Outline each Plasmodium vivax-infected red blood cell.
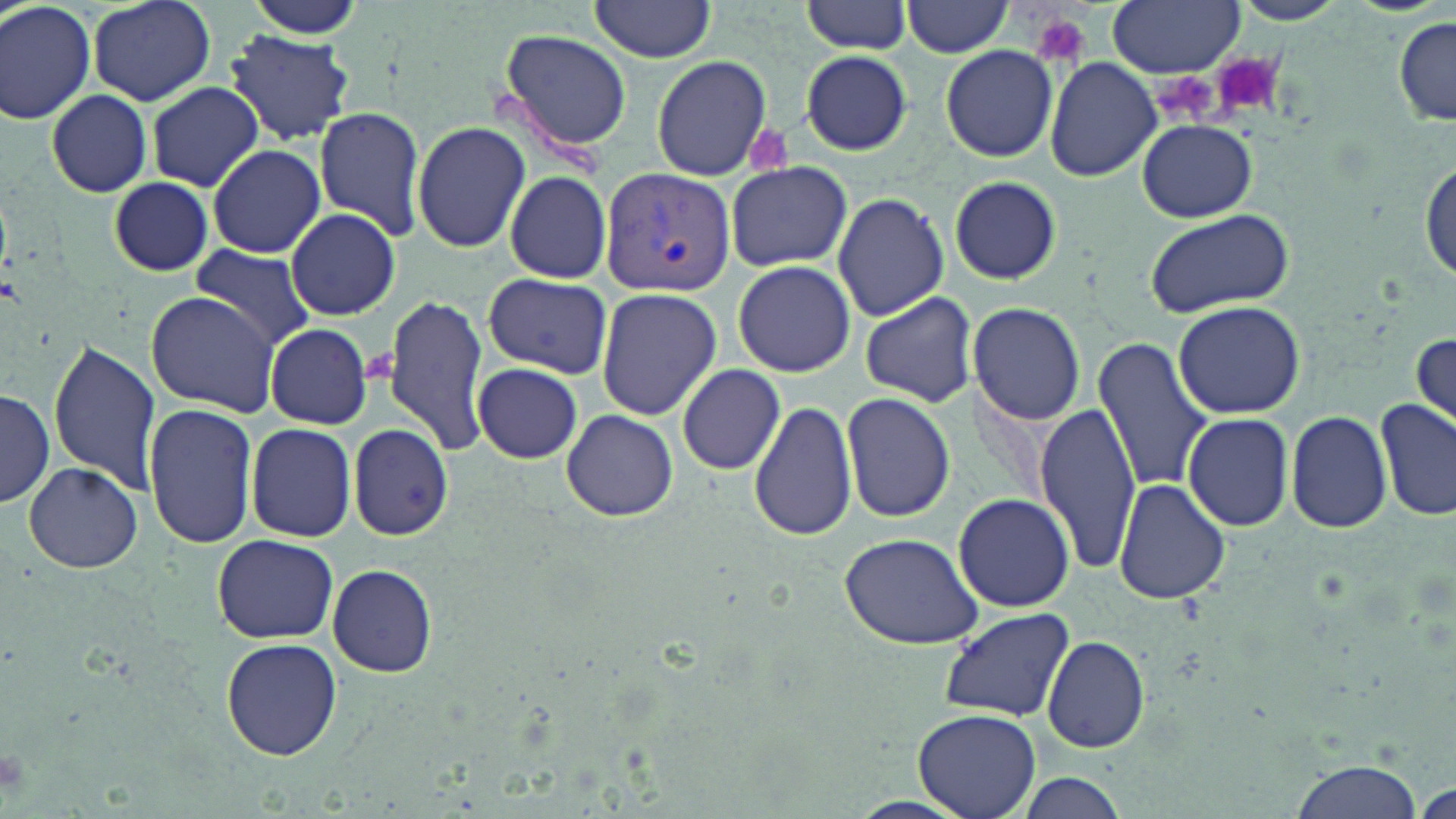

Approximate bounding boxes as [x1, y1, x2, y2] in pixels.
Plasmodium vivax-infected red blood cells: [599, 167, 736, 295].

{
  "slide_level_diagnosis": "Plasmodium vivax",
  "platelet_locations": "approximate bounding boxes as [x1, y1, x2, y2] in pixels: [1031, 14, 1090, 67], [1214, 54, 1283, 116], [1152, 69, 1220, 126]",
  "modality": "optical microscopy",
  "magnification": "1000x",
  "stain": "May-Grünwald-Giemsa",
  "image_size": "1456×819 pixels",
  "uninfected_red_blood_cell_locations": "approximate bounding boxes as [x1, y1, x2, y2] in pixels: [0, 0, 97, 124], [87, 0, 216, 106], [243, 0, 367, 39], [801, 0, 914, 55], [1229, 0, 1347, 26], [587, 1, 719, 63], [902, 1, 1016, 56], [1108, 2, 1243, 75], [1393, 19, 1455, 125], [499, 27, 632, 155], [222, 30, 356, 143], [940, 45, 1059, 162], [801, 51, 911, 155], [652, 57, 772, 179], [1043, 57, 1161, 181], [146, 82, 263, 191], [45, 89, 152, 197], [314, 106, 430, 243], [1139, 119, 1257, 221], [411, 120, 530, 253], [206, 144, 326, 258], [1420, 158, 1454, 286], [725, 162, 851, 271], [503, 170, 612, 283], [950, 176, 1060, 285], [108, 177, 214, 275], [833, 191, 950, 321], [286, 209, 401, 319], [1143, 209, 1296, 317], [187, 247, 316, 355], [729, 260, 858, 379], [483, 273, 612, 379], [595, 286, 722, 420], [146, 290, 281, 415], [860, 290, 979, 407], [381, 293, 492, 456], [1171, 301, 1306, 420], [967, 302, 1086, 425], [265, 324, 372, 428], [1413, 332, 1455, 431], [1092, 337, 1211, 493], [47, 341, 159, 492], [473, 363, 583, 462], [676, 363, 786, 475], [0, 385, 53, 509], [842, 391, 955, 523], [750, 397, 859, 543], [1375, 397, 1455, 521], [144, 401, 259, 550], [1035, 402, 1140, 573], [561, 409, 678, 522], [1285, 409, 1392, 534], [1183, 412, 1296, 532], [244, 422, 357, 541], [347, 424, 453, 543], [22, 462, 143, 572], [1113, 478, 1232, 606], [952, 493, 1074, 611], [837, 533, 988, 649], [212, 535, 340, 643], [328, 563, 438, 678], [939, 607, 1074, 722], [964, 615, 1158, 739], [1041, 636, 1151, 753], [221, 638, 341, 760], [915, 707, 1040, 818], [1283, 761, 1425, 819], [1009, 772, 1133, 818]",
  "field_of_view": "single",
  "preparation": "thin blood smear"
}